Assess this cell for malaria.
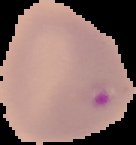
Parasitized.

Summary:
  - Image size: 136×145 pixels
  - Preparation: thin blood smear
  - Image type: segmented cell region on a black background